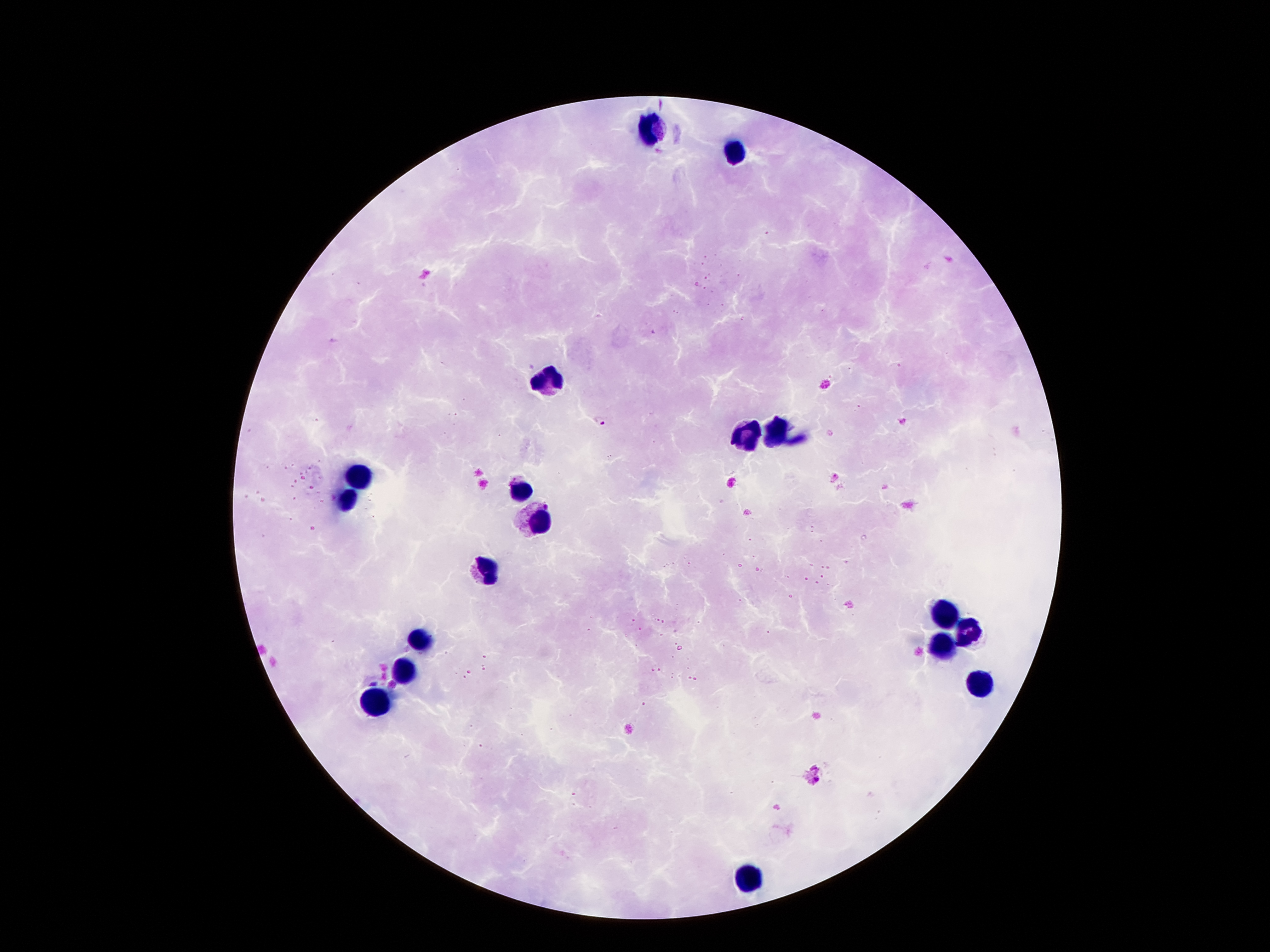
Approximate centers as (x, y) in pixels.
Summary:
  - Plasmodium parasite locations: (601, 423), (835, 477)
  - Leukocyte locations: (649, 128), (733, 151), (546, 378), (781, 428), (748, 435), (357, 472), (521, 491), (344, 500), (540, 521), (485, 567), (943, 611), (966, 634), (416, 642), (941, 647), (403, 672), (979, 682), (376, 705), (750, 873)
  - Capture: smartphone camera through the microscope eyepiece
  - Field of view: one from this slide
  - Stain: Giemsa
  - Patient malaria status: infected with Plasmodium falciparum
  - Magnification: 100x
  - Image size: 1270×952 pixels
  - Preparation: thick blood smear